Locate every malaria parasite.
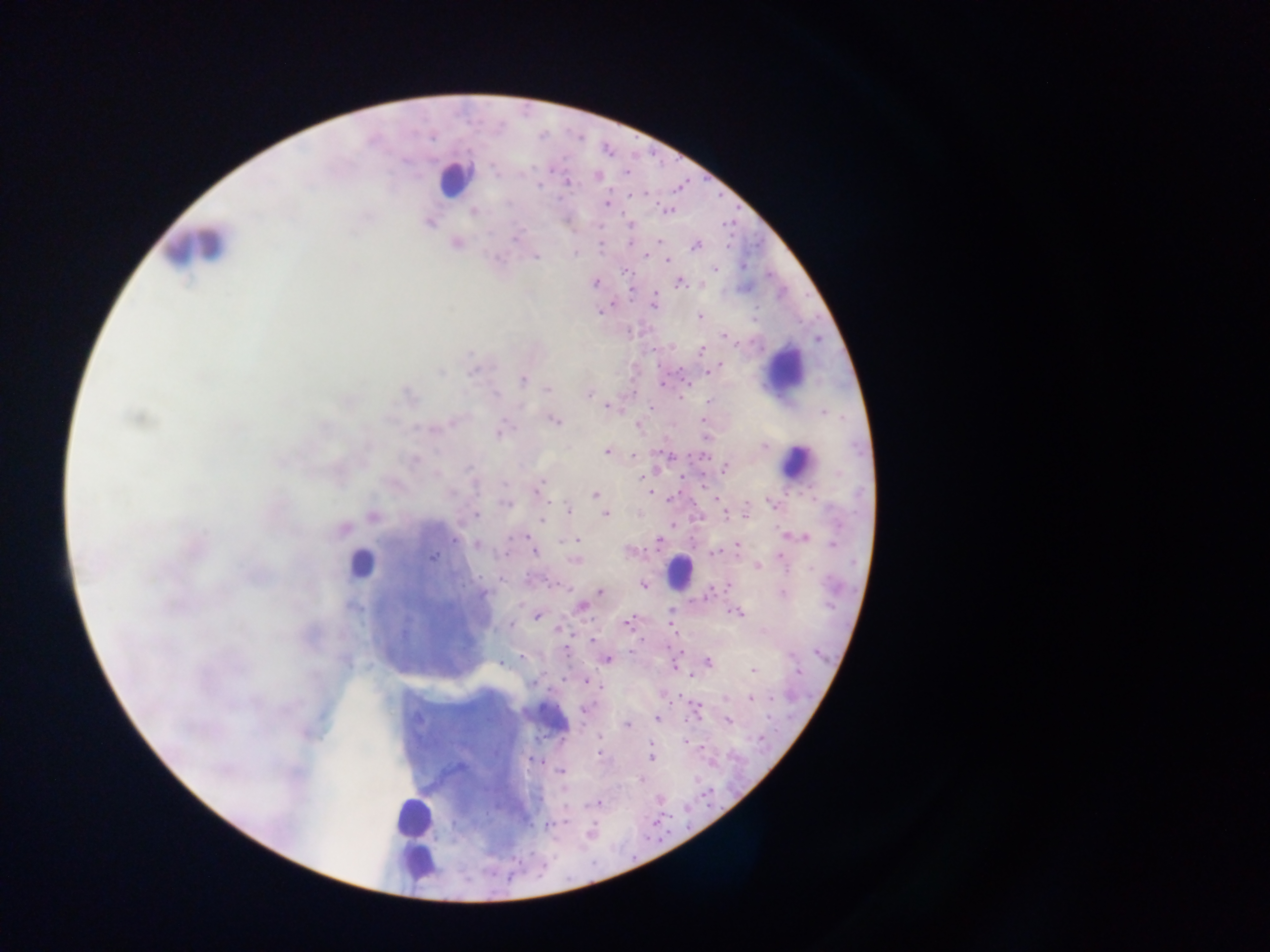

Approximate centers as [x, y] in pixels.
Malaria parasites: [404, 161], [495, 172], [626, 173], [597, 175], [569, 182], [539, 185], [608, 203], [667, 209], [474, 212], [430, 223], [599, 226], [515, 238], [659, 240], [456, 243], [631, 243], [695, 246], [600, 247], [575, 252], [645, 255], [536, 256], [668, 260], [743, 265], [715, 269], [625, 271], [595, 283], [680, 283], [655, 302], [599, 312], [699, 316], [640, 332], [724, 334], [656, 348], [701, 350], [720, 364], [710, 371], [440, 372], [471, 372], [522, 379], [664, 381], [547, 389], [589, 394], [496, 395], [681, 397], [709, 401], [606, 406], [651, 408], [823, 412], [137, 418], [555, 421], [453, 422], [425, 429], [500, 432], [764, 446], [606, 452], [634, 456], [414, 460], [725, 468], [470, 469], [682, 473], [642, 477], [505, 484], [475, 486], [539, 487], [648, 492], [595, 494], [772, 502], [507, 504], [725, 508], [569, 510], [746, 512], [605, 514], [476, 515], [372, 516], [543, 520], [344, 529], [525, 537], [804, 538], [576, 540], [455, 541], [659, 541], [833, 543], [477, 545], [736, 545], [534, 550], [628, 551], [714, 553], [432, 557], [574, 561], [758, 566], [728, 584], [644, 586], [600, 592], [483, 594], [783, 594], [707, 595], [581, 607], [671, 613], [737, 613], [537, 616], [628, 622], [510, 625], [559, 629], [592, 640], [816, 653], [522, 657], [607, 659], [707, 661], [503, 664], [753, 670], [797, 671], [585, 681], [533, 683], [601, 687], [726, 698], [752, 698], [585, 708], [657, 718], [729, 721], [627, 725], [598, 736], [686, 742], [650, 744], [598, 755], [652, 757], [533, 760], [561, 771], [641, 779], [599, 802], [549, 826], [590, 832].

Leukocyte locations: [454, 178], [191, 244], [787, 365], [797, 462], [361, 564], [680, 571], [413, 816], [415, 860]. Image is 1270×952 pixels. One field of view. Thick blood film. Photographed through a microscope with a mobile-phone camera. Collected in Ghana.